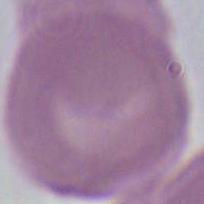

{
  "identification": "red blood cell",
  "modality": "photomicrograph",
  "magnification": "1000x"
}